Give a bounding box for every malaria parasite.
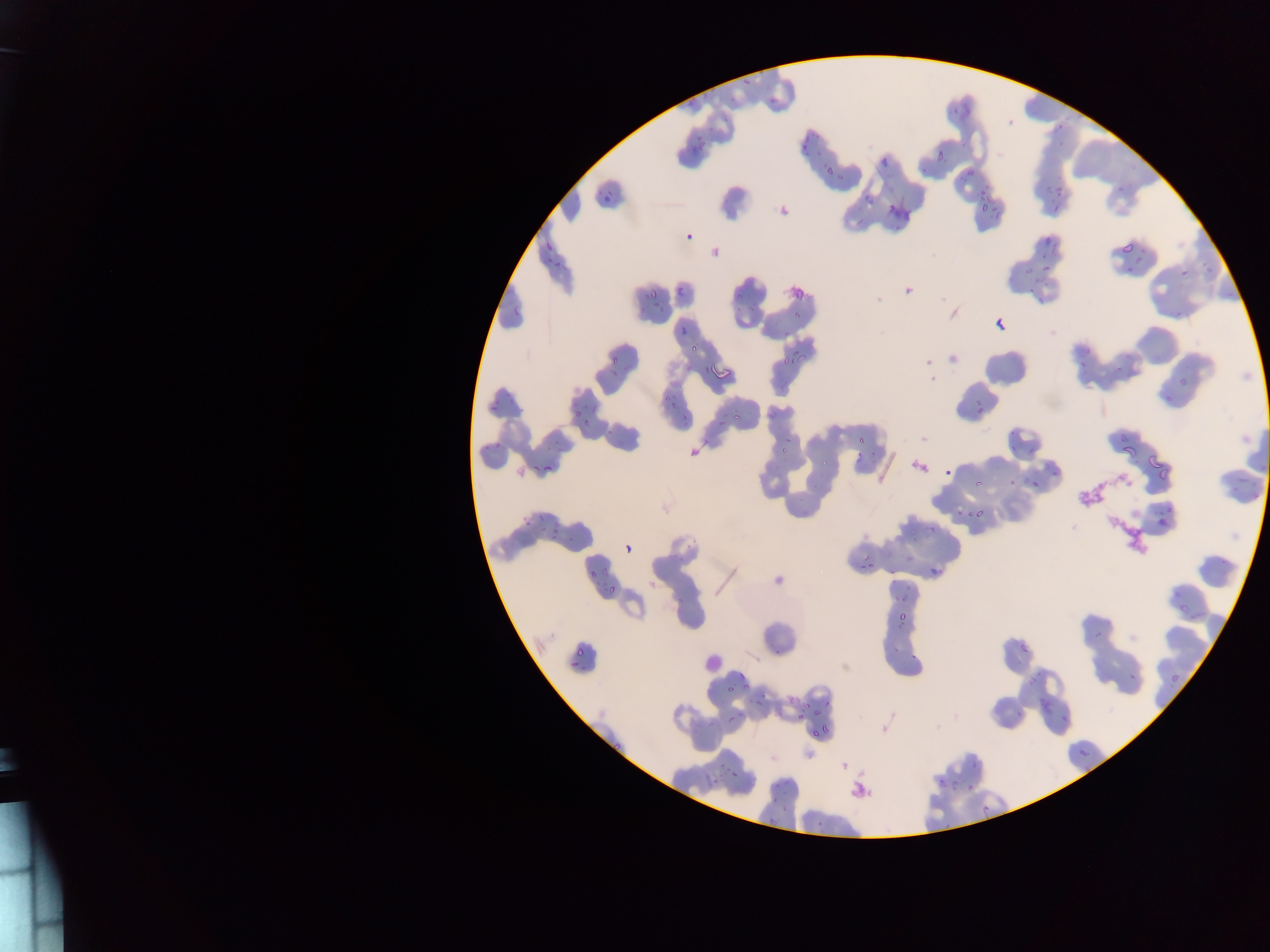
Approximate bounding boxes as [left, top, right, bottom] in pixels.
Malaria parasites: [768, 96, 776, 105], [1056, 123, 1064, 131], [682, 127, 714, 153], [801, 139, 811, 151], [932, 140, 952, 165], [872, 152, 890, 165], [960, 161, 973, 176], [823, 165, 835, 176], [854, 175, 877, 203], [979, 186, 1002, 216], [886, 187, 921, 223], [600, 192, 616, 205], [1054, 204, 1063, 213], [1053, 207, 1061, 216], [1038, 231, 1056, 248], [682, 232, 689, 241], [545, 242, 552, 252], [1120, 242, 1133, 255], [1043, 260, 1063, 278], [1180, 268, 1189, 277], [788, 282, 811, 298], [677, 285, 685, 294], [728, 287, 750, 304], [650, 290, 660, 300], [788, 312, 795, 320], [996, 319, 1005, 328], [688, 332, 705, 356], [781, 340, 814, 366], [604, 346, 630, 366], [715, 366, 731, 386], [650, 381, 696, 416], [486, 387, 510, 415], [728, 409, 745, 422], [582, 415, 599, 431], [857, 417, 878, 449], [1033, 432, 1043, 440], [1143, 440, 1160, 477], [1110, 442, 1133, 463], [944, 451, 966, 481], [528, 460, 540, 470], [542, 463, 555, 471], [1005, 475, 1018, 491], [1028, 475, 1045, 493], [973, 477, 983, 487], [1150, 504, 1177, 529], [952, 506, 978, 518], [920, 517, 941, 535], [547, 528, 559, 539], [625, 541, 635, 558], [843, 548, 870, 579], [936, 557, 957, 572], [587, 569, 596, 579], [600, 579, 620, 595], [895, 603, 910, 619], [1178, 603, 1190, 614], [1087, 620, 1116, 641], [1019, 626, 1040, 652], [569, 636, 594, 662], [774, 646, 784, 655], [1122, 665, 1134, 678], [1019, 668, 1042, 683], [1169, 671, 1181, 687], [739, 673, 747, 683], [720, 684, 737, 700], [792, 693, 819, 720], [762, 695, 779, 710], [1039, 699, 1049, 711], [726, 711, 743, 724], [1061, 714, 1070, 724], [801, 719, 827, 744], [603, 737, 629, 756], [1079, 748, 1089, 757], [722, 755, 742, 770], [933, 778, 954, 790], [771, 780, 780, 789], [967, 784, 976, 792], [815, 818, 825, 828] | approximate [x, y] pixel centers of objects too small to bound: [1121, 188], [928, 361].

Summary:
  - Leukocyte locations: [692, 647, 716, 671], [701, 651, 723, 673]
  - Capture: mobile-phone photograph through a microscope
  - Country: Ghana
  - Field of view: single
  - Image size: 1270×952 pixels
  - Preparation: thin blood smear